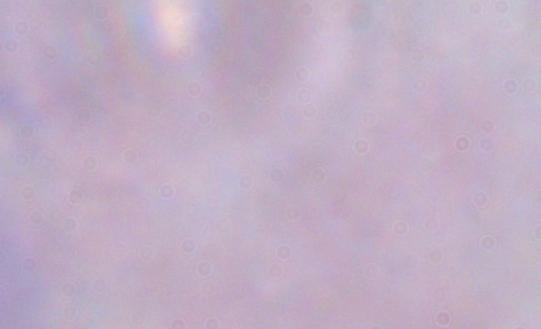

magnification = 1000x
modality = micrograph
identification = trypanosome